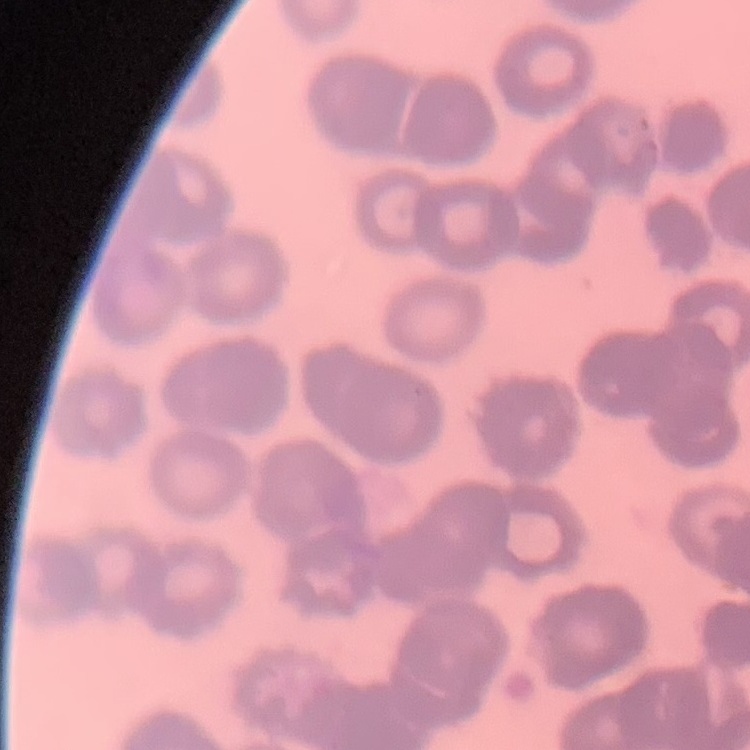

erythrocyte morphology = rouleaux formation
image type = square crop of a larger photomicrograph
stain = Field's or Giemsa
preparation = thin blood film